Locate every Trypanosoma brucei.
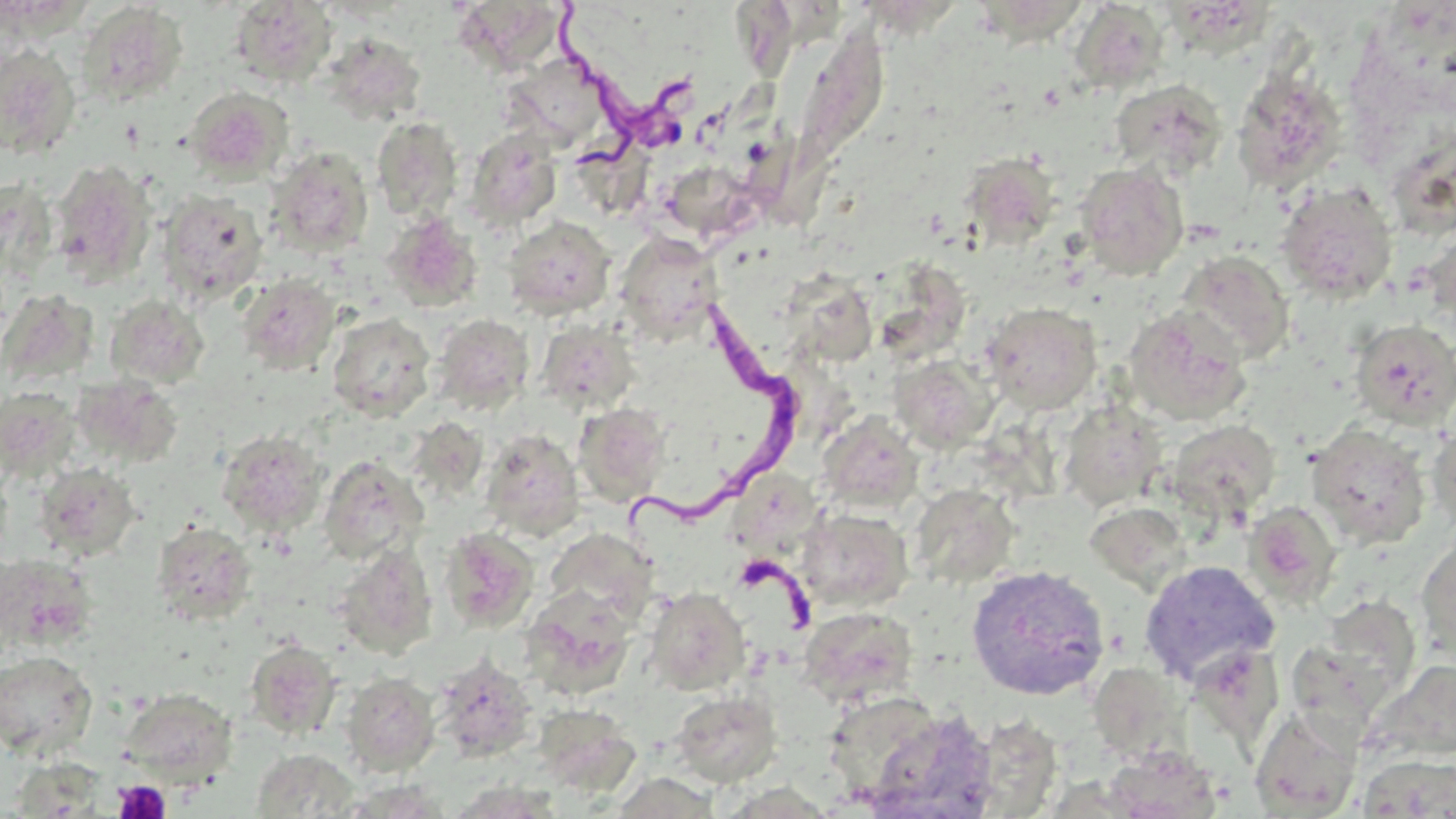

Approximate bounding boxes as [x1, y1, x2, y2] in pixels.
Trypanosoma brucei: [554, 10, 716, 159], [625, 292, 811, 534].

Summary:
  - Uninfected red blood cell locations: [865, 0, 957, 45], [983, 0, 1103, 62], [229, 1, 337, 88], [76, 3, 189, 107], [465, 3, 558, 74], [733, 3, 810, 97], [1070, 3, 1171, 93], [1160, 5, 1287, 69], [796, 19, 898, 183], [319, 32, 427, 126], [0, 45, 82, 159], [502, 54, 614, 152], [1232, 70, 1347, 195], [1110, 79, 1228, 179], [184, 86, 294, 184], [371, 116, 463, 221], [466, 127, 562, 229], [576, 135, 662, 210], [1396, 136, 1452, 233], [266, 146, 374, 258], [761, 151, 846, 229], [960, 153, 1064, 248], [49, 161, 157, 286], [1075, 162, 1189, 280], [673, 169, 756, 239], [1275, 181, 1398, 303], [156, 190, 268, 303], [382, 212, 483, 312], [502, 215, 616, 320], [1423, 227, 1456, 336], [615, 232, 724, 343], [1178, 250, 1295, 363], [238, 274, 341, 375], [786, 276, 880, 368], [105, 294, 209, 388], [982, 302, 1102, 414], [1124, 305, 1253, 426], [327, 312, 436, 421], [432, 314, 534, 414], [536, 318, 641, 415], [1350, 320, 1456, 430], [888, 354, 997, 451], [75, 377, 182, 468], [0, 387, 80, 477], [1060, 400, 1166, 511], [574, 403, 671, 507], [817, 413, 924, 515], [1167, 419, 1282, 519], [1427, 419, 1456, 533], [981, 422, 1075, 495], [1305, 423, 1432, 549], [217, 428, 328, 537], [479, 429, 584, 541], [318, 455, 427, 564], [0, 458, 13, 563], [35, 461, 142, 561], [911, 484, 1020, 587], [1244, 501, 1343, 607], [795, 508, 912, 613], [151, 521, 256, 625], [1416, 526, 1456, 663], [439, 527, 538, 632], [546, 528, 659, 623], [333, 543, 438, 659], [0, 555, 96, 650], [1139, 559, 1280, 687], [965, 565, 1110, 700], [643, 586, 751, 694], [520, 589, 637, 697], [1315, 596, 1424, 712], [798, 605, 919, 708], [245, 640, 342, 739], [1188, 643, 1285, 754], [0, 651, 98, 758], [430, 653, 538, 761], [1095, 658, 1188, 763], [1371, 660, 1456, 762], [341, 672, 440, 776], [121, 688, 238, 783], [668, 689, 783, 787], [823, 691, 943, 801], [534, 704, 640, 797], [1250, 706, 1362, 818], [864, 709, 1000, 819], [1102, 744, 1223, 818], [251, 748, 359, 818], [1357, 755, 1456, 816], [613, 772, 722, 818]
  - Platelet locations: [112, 779, 171, 819]
  - Slide-level diagnosis: Trypanosoma brucei
  - Image size: 1456×819 pixels
  - Field of view: one of a larger specimen
  - Modality: light microscopy
  - Preparation: thin blood smear
  - Stain: May-Grünwald-Giemsa
  - Magnification: 1000x